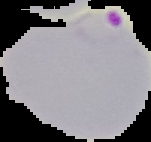
image type = segmented cell region with the area outside set to black
image size = 151×142 pixels
malaria status = parasitized
preparation = thin blood film